Assess this cell for malaria.
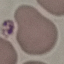

Uninfected.

Summary:
  - Stain: Giemsa
  - Preparation: thin blood smear
  - Capture: smartphone camera at the microscope eyepiece
  - Image type: cell patch, automatically extracted from a larger field of view and resized to 64 × 64 pixels